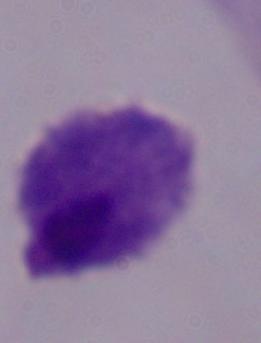 1000x magnification. Micrograph. A trichomonad is shown.